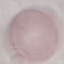
Summary:
  - Malaria status: uninfected
  - Preparation: thin smear
  - Capture: smartphone through the microscope eyepiece
  - Stain: Giemsa
  - Image type: cell patch, automatically extracted from a larger field of view and resized to 64 × 64 pixels